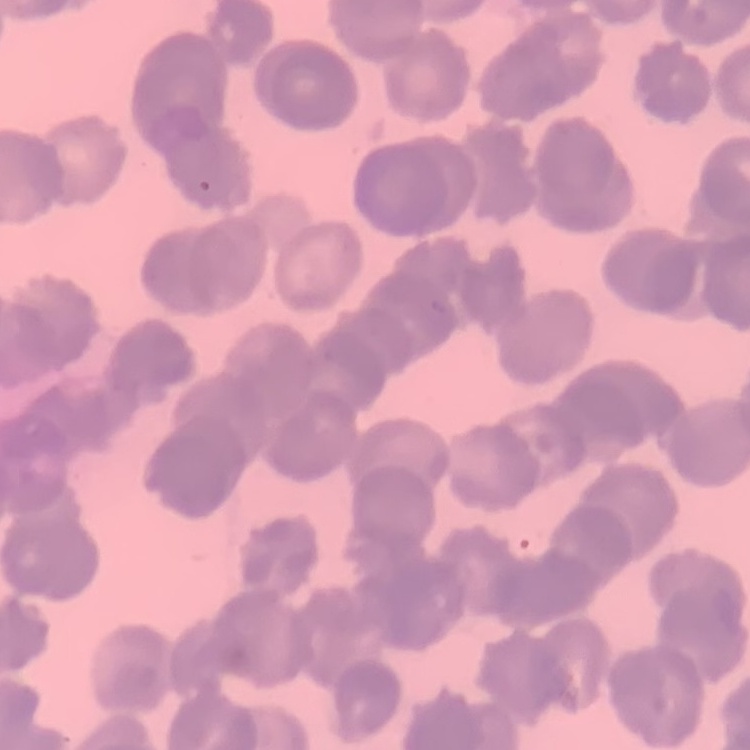

Summary:
  - Red blood cell morphology: rouleaux formation
  - Stain: Field's or Giemsa
  - Image type: one tile cut from a larger photomicrograph
  - Preparation: thin blood film